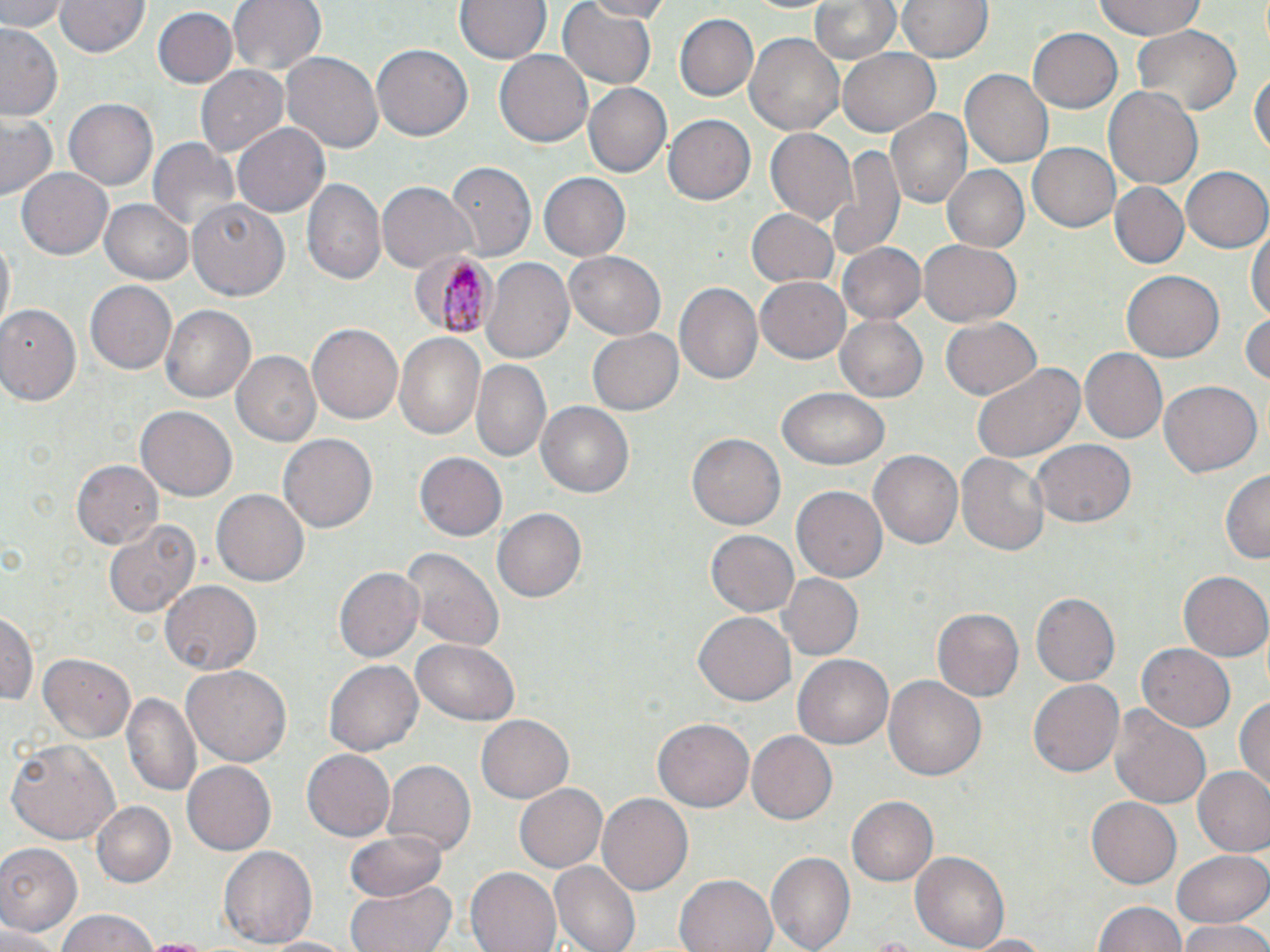

slide-level diagnosis = Plasmodium malariae
image size = 1270×952 pixels
modality = light microscopy
field of view = single
stain = May-Grünwald-Giemsa
preparation = thin blood smear
magnification = 1000x
uninfected red blood cell locations = approximate bounding boxes as (x1, y1, x2, y2) in pixels: (3, 0, 67, 32), (56, 0, 150, 59), (228, 0, 327, 77), (455, 0, 549, 64), (577, 0, 675, 21), (806, 0, 902, 69), (898, 0, 993, 63), (1092, 0, 1208, 40), (558, 3, 658, 89), (154, 6, 236, 86), (677, 13, 759, 102), (1, 24, 64, 121), (1128, 26, 1242, 121), (1027, 27, 1123, 112), (743, 31, 845, 136), (371, 44, 470, 142), (836, 47, 941, 136), (495, 50, 593, 148), (281, 52, 384, 154), (1250, 64, 1269, 160), (197, 66, 289, 157), (961, 70, 1053, 167), (581, 83, 672, 178), (1103, 84, 1203, 193), (65, 99, 157, 190), (884, 106, 973, 211), (2, 112, 60, 201), (664, 115, 756, 204), (231, 123, 331, 219), (765, 128, 855, 226), (148, 137, 241, 238), (1026, 142, 1119, 232), (829, 146, 904, 260), (447, 163, 535, 260), (16, 166, 113, 260), (944, 166, 1028, 251), (1180, 166, 1270, 254), (537, 172, 630, 261), (302, 179, 386, 287), (379, 182, 476, 272), (1109, 182, 1189, 270), (102, 198, 194, 283), (188, 200, 291, 301), (746, 207, 840, 288), (1249, 224, 1269, 329), (1, 239, 15, 327), (918, 239, 1023, 326), (836, 240, 925, 325), (564, 252, 666, 340), (482, 257, 575, 366), (1122, 269, 1225, 363), (756, 276, 850, 364), (85, 280, 178, 376), (674, 282, 764, 385), (162, 305, 256, 405), (0, 306, 81, 407), (1242, 312, 1269, 389), (835, 314, 929, 403), (942, 318, 1041, 399), (307, 323, 404, 427), (589, 329, 684, 416), (393, 332, 487, 442), (1078, 349, 1166, 442), (232, 350, 321, 445), (471, 359, 552, 463), (972, 361, 1086, 466), (1157, 378, 1262, 475), (778, 388, 890, 471), (536, 400, 636, 500), (137, 407, 237, 500), (687, 432, 787, 532), (278, 434, 377, 534), (1032, 439, 1136, 529), (869, 449, 962, 549), (416, 451, 509, 542), (956, 452, 1050, 558), (72, 459, 163, 551), (1221, 468, 1269, 568), (792, 485, 887, 583), (213, 489, 308, 586), (494, 510, 586, 601), (102, 515, 201, 620), (706, 529, 800, 619), (401, 546, 503, 653), (334, 567, 424, 662), (1179, 572, 1270, 663), (776, 573, 864, 661), (163, 580, 261, 674), (1030, 592, 1121, 688), (931, 606, 1023, 701), (0, 607, 37, 709), (693, 610, 796, 707), (412, 640, 519, 724), (1137, 642, 1235, 731), (40, 652, 137, 741), (793, 654, 893, 750), (324, 659, 423, 757), (182, 664, 291, 766), (884, 676, 987, 783), (1027, 678, 1124, 780), (125, 690, 199, 796), (1234, 696, 1270, 795), (1108, 703, 1212, 810), (476, 713, 574, 804), (653, 717, 755, 813), (749, 732, 837, 822), (7, 739, 121, 845), (303, 747, 393, 841), (181, 761, 276, 855), (382, 761, 474, 855), (1194, 765, 1270, 855), (516, 781, 608, 873), (595, 793, 692, 897), (1086, 794, 1181, 887), (847, 796, 939, 885), (91, 801, 176, 886), (344, 828, 448, 902), (0, 842, 83, 937), (219, 843, 319, 950), (1172, 846, 1269, 929), (765, 849, 856, 949), (910, 850, 1010, 952), (550, 861, 641, 952), (467, 868, 561, 952), (674, 874, 777, 952), (347, 880, 456, 952), (1094, 898, 1189, 952), (55, 908, 162, 952), (1178, 922, 1270, 952), (0, 924, 61, 952), (964, 933, 1056, 951), (262, 934, 360, 951), (139, 937, 215, 952)
Plasmodium malariae-infected red blood cell locations = approximate bounding boxes as (x1, y1, x2, y2) in pixels: (410, 249, 499, 338)